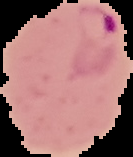

Summary:
  - Preparation: thin blood smear
  - Malaria status: parasitized
  - Image size: 133×157 pixels
  - Image type: cell region segmented out of the field of view; surrounding area masked to black